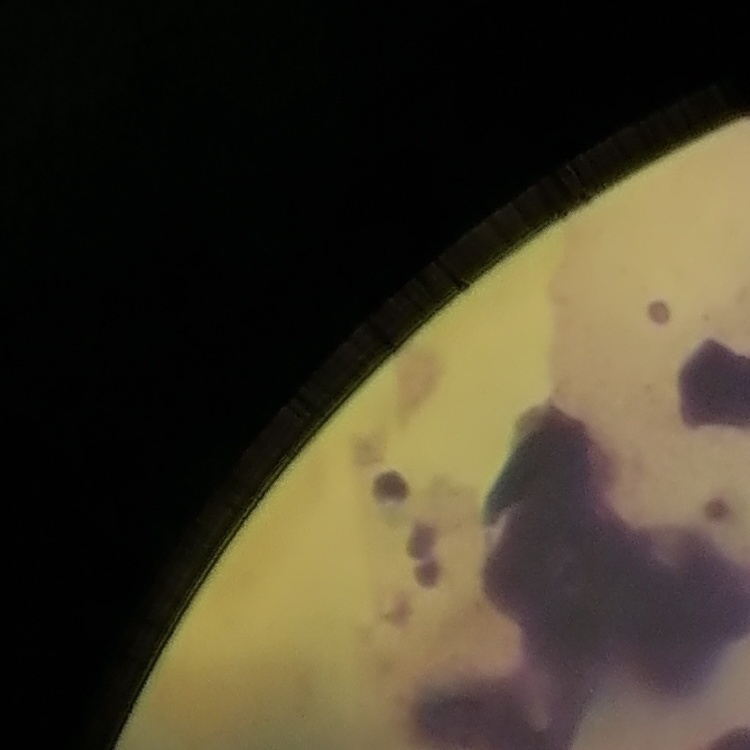
Summary:
  - Erythrocyte morphology: rouleaux formation
  - Stain: Field's or Giemsa
  - Image type: one tile cut from a larger photomicrograph
  - Preparation: thin peripheral smear